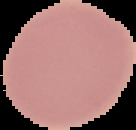 The area outside the segmented cell region is set to black. Image is 136×130 pixels. Result: no Plasmodium parasites seen. From a thin blood smear.